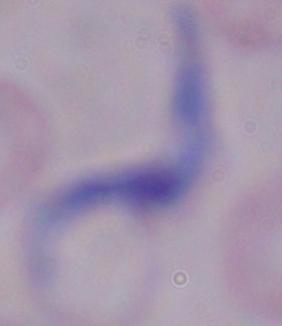

modality = photomicrograph
identification = trypanosome
magnification = 1000x